Locate every Plasmodium parasite.
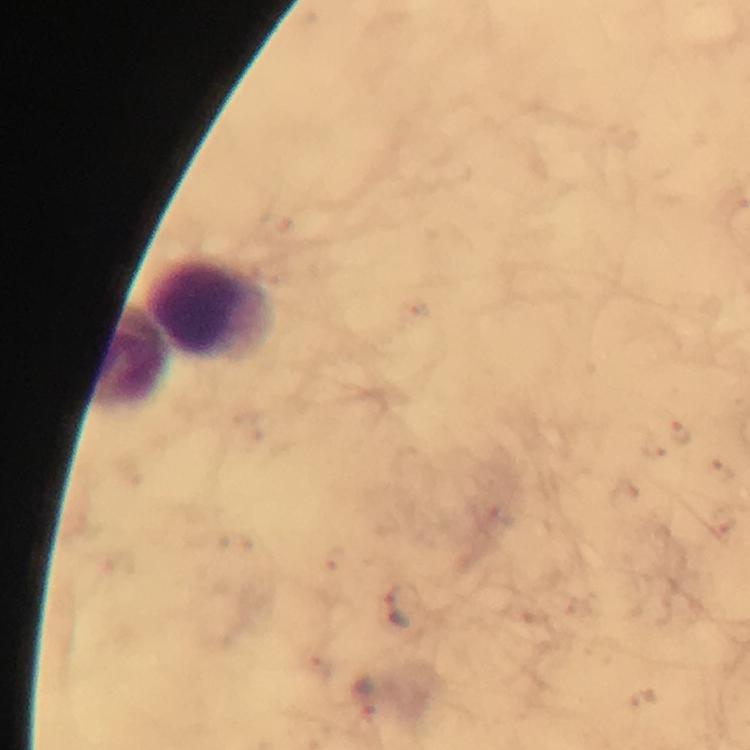

Approximate object centers, in pixels from the top-left corner.
Plasmodium parasites: (x=403, y=604).

context = from a malaria diagnostic workup
leukocyte locations = approximate object centers, in pixels from the top-left corner: (x=210, y=311), (x=129, y=359)
image size = 750×750 pixels
immersion oil = applied
magnification = 100x
cropped from = one field of view
capture = smartphone photograph through a microscope
preparation = thick blood film
stain = Giemsa